Outline each Plasmodium ovale-infected red blood cell.
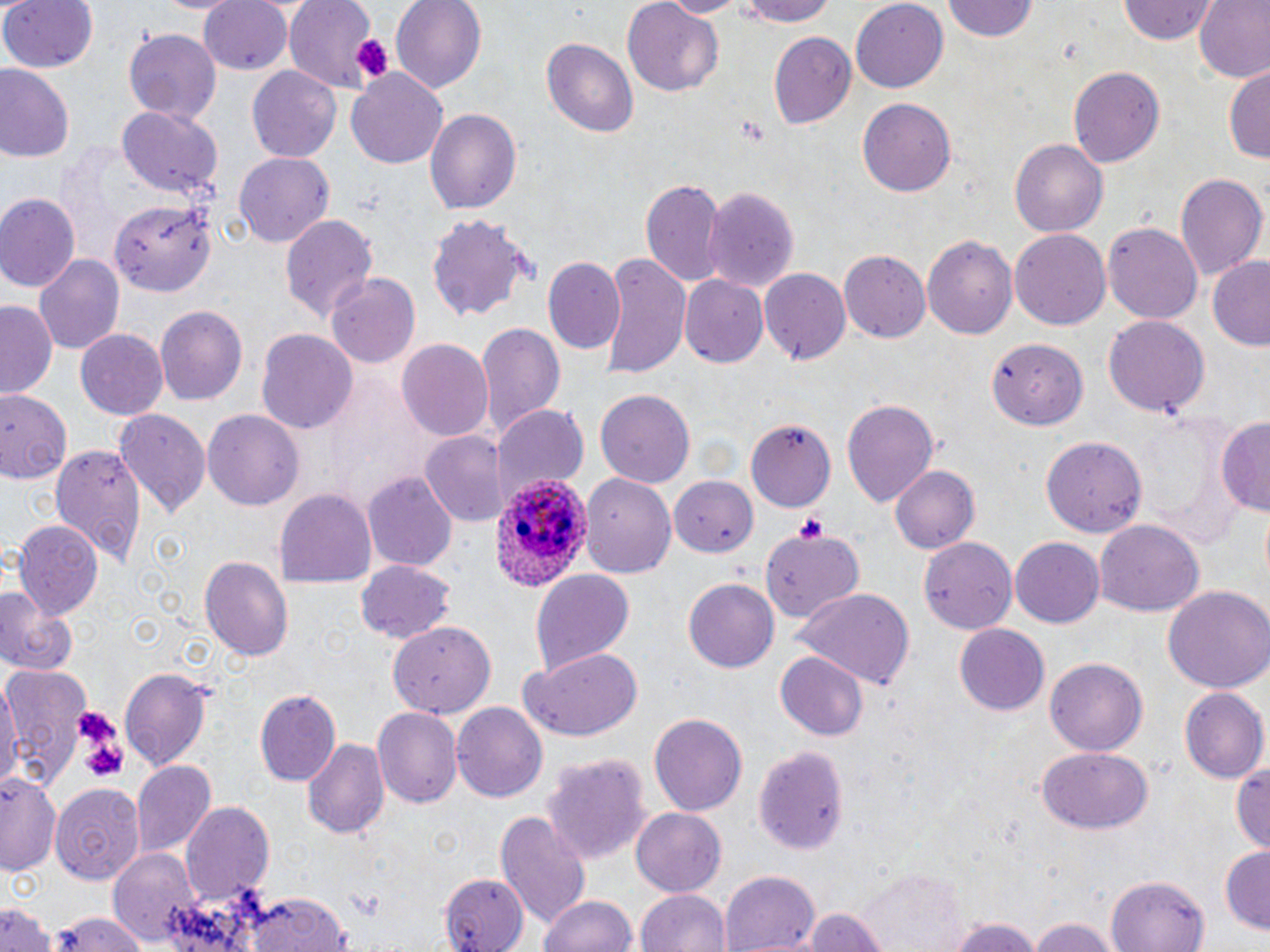
Approximate bounding boxes as (x1, y1, x2, y2) in pixels.
Plasmodium ovale-infected red blood cells: (493, 475, 593, 591).

slide_level_diagnosis: Plasmodium ovale
image_size: 1270×952 pixels
preparation: thin blood smear
modality: light microscopy
platelet_locations: 'approximate bounding boxes as (x1, y1, x2, y2) in pixels: (355, 35, 391, 78), (795, 511, 831, 541), (76, 709, 123, 743), (81, 728, 128, 782)'
stain: May-Grünwald-Giemsa
magnification: 1000x
uninfected_red_blood_cell_locations: 'approximate bounding boxes as (x1, y1, x2, y2) in pixels: (153, 0, 240, 15), (199, 0, 295, 73), (281, 0, 373, 96), (390, 0, 486, 91), (657, 0, 750, 17), (737, 0, 836, 28), (850, 0, 947, 91), (944, 0, 1039, 43), (1192, 0, 1270, 84), (0, 1, 99, 73), (1116, 1, 1220, 45), (619, 2, 723, 97), (122, 30, 221, 123), (768, 30, 858, 126), (544, 38, 638, 139), (246, 64, 341, 162), (0, 65, 75, 163), (1067, 65, 1166, 167), (1223, 66, 1269, 164), (347, 68, 449, 169), (857, 97, 958, 197), (119, 105, 221, 195), (422, 106, 522, 215), (1010, 138, 1106, 239), (233, 152, 335, 247), (1175, 170, 1267, 282), (640, 177, 725, 286), (703, 183, 800, 294), (0, 194, 79, 294), (111, 201, 220, 297), (280, 212, 379, 322), (426, 213, 532, 323), (1104, 221, 1201, 324), (1010, 229, 1110, 332), (923, 236, 1017, 339), (838, 250, 930, 344), (601, 252, 689, 376), (34, 254, 124, 356), (1207, 256, 1270, 351), (543, 258, 624, 356), (759, 267, 849, 365), (329, 274, 420, 368), (677, 275, 768, 368), (1, 300, 57, 398), (155, 305, 247, 405), (1104, 316, 1209, 417), (473, 320, 564, 437), (76, 328, 166, 419), (256, 329, 358, 434), (397, 338, 496, 441), (993, 340, 1086, 428), (0, 387, 71, 482), (596, 389, 693, 491), (842, 397, 940, 507), (495, 406, 590, 497), (201, 407, 306, 509), (113, 408, 211, 518), (64, 415, 193, 545), (1215, 415, 1270, 517), (750, 419, 836, 510), (421, 429, 505, 527), (1041, 436, 1147, 539), (50, 441, 147, 565), (890, 465, 979, 552), (363, 472, 458, 573), (582, 474, 674, 579), (670, 478, 756, 554), (274, 487, 376, 586), (1095, 519, 1203, 619), (12, 520, 102, 619), (758, 522, 868, 621), (919, 537, 1017, 635), (1009, 537, 1103, 629), (200, 555, 294, 662), (355, 560, 454, 642), (528, 569, 633, 677), (682, 578, 779, 673), (1163, 584, 1270, 693), (795, 587, 916, 689), (0, 588, 79, 677), (387, 622, 496, 715), (955, 624, 1050, 715), (520, 649, 644, 744), (774, 650, 869, 740), (1046, 655, 1148, 755), (3, 665, 91, 787), (119, 668, 211, 770), (0, 681, 19, 795), (1181, 687, 1268, 783), (255, 689, 341, 784), (275, 693, 379, 814), (453, 702, 547, 804), (374, 705, 462, 809), (648, 713, 749, 815), (302, 737, 388, 841), (755, 745, 849, 856), (1037, 747, 1155, 834), (542, 751, 649, 875), (1232, 757, 1270, 855), (131, 759, 215, 856), (1, 771, 61, 875), (51, 783, 145, 886), (182, 803, 274, 905), (632, 808, 726, 894), (494, 811, 591, 928), (1219, 845, 1270, 933), (108, 848, 199, 949), (861, 869, 967, 952), (721, 870, 820, 951), (444, 874, 522, 952), (1106, 876, 1210, 952), (637, 888, 730, 952), (232, 889, 356, 952), (538, 893, 636, 952), (0, 895, 54, 952), (797, 908, 892, 952), (50, 911, 154, 952), (1027, 914, 1117, 952), (948, 916, 1045, 952)'
field_of_view: one of a larger specimen